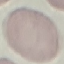
Result: no malaria parasites seen. Acquired by smartphone through the microscope eyepiece. Thin smear of blood. Automatically extracted cell patch, resized to 64 × 64 pixels. Giemsa-stained preparation.